Assess this cell for malaria.
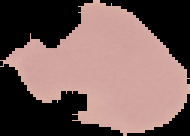
It is uninfected.

Summary:
  - Image size: 190×136 pixels
  - Image type: segmented cell region with the area outside set to black
  - Preparation: thin blood smear